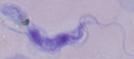
Photomicrograph. Captured at 1000x magnification. A trypanosome is seen.